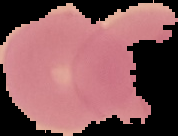
From a thin blood smear. Result: no malaria parasites detected. Image is 178×136 pixels. Cell region segmented out of the field of view; the surrounding area is masked to black.